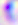 400x magnification. Micrograph. Toxoplasma gondii is seen.